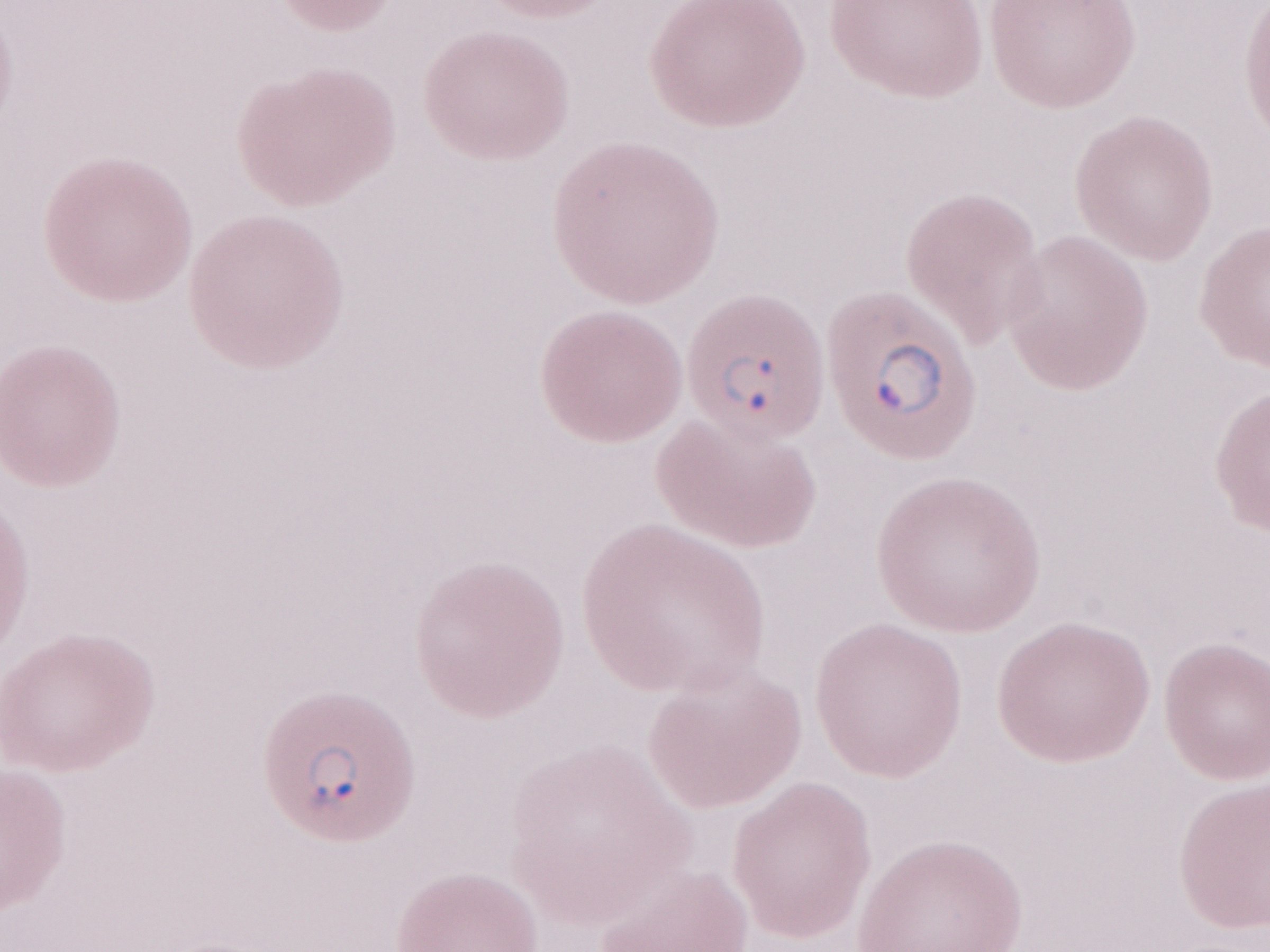
Olympus BX43 microscope and DP73 digital camera. Thin blood smear. May-Grünwald-Giemsa (MGG) stain. Magnification: 1,000x. Patient diagnosis: malaria infection. Single field of view. Image is 1270×952 pixels.